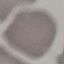

Summary:
  - Result: no malaria parasites seen
  - Capture: smartphone through the microscope eyepiece
  - Image type: automatically extracted cell patch, resized to 64 × 64 pixels
  - Stain: Giemsa
  - Preparation: thin blood film